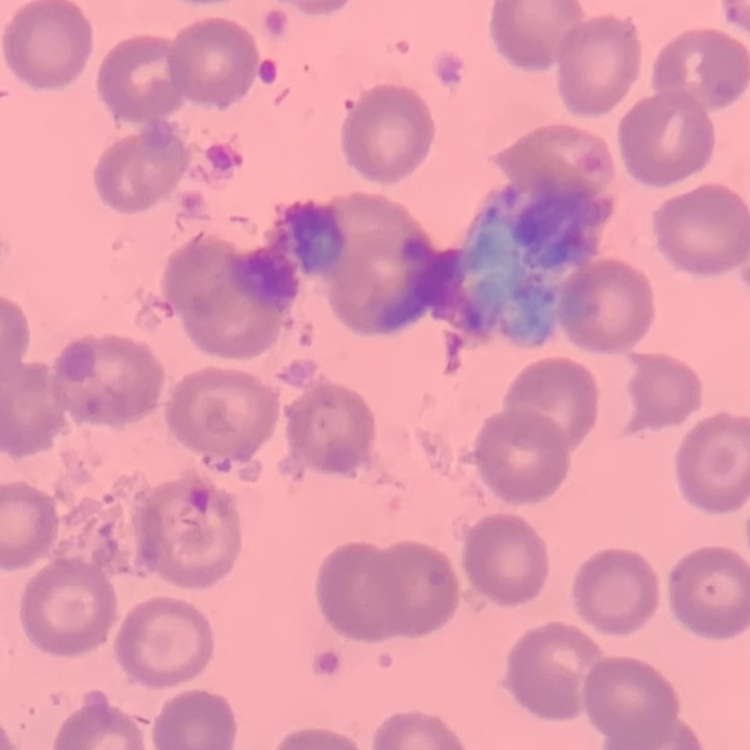
Summary:
  - Erythrocyte morphology: no rouleaux formation
  - Image type: square crop of a larger photomicrograph
  - Stain: Field's or Giemsa
  - Preparation: thin blood smear